State which parasite is depicted.
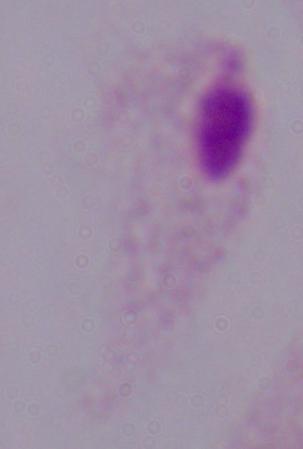

A trichomonad.

Photomicrograph. Captured at 1000x magnification.